Identify the parasite.
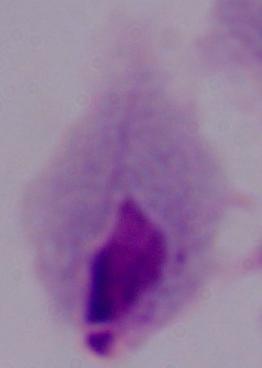

A trichomonad.

Summary:
  - Modality: micrograph
  - Magnification: 1000x